Classify this cell by malaria status.
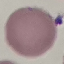

It is uninfected.

Thin smear of blood. Automatically extracted cell patch, resized to 64 × 64 pixels. Photographed with a smartphone camera at the microscope eyepiece. Giemsa-stained preparation.